Point out each Plasmodium parasite and each leukocyte.
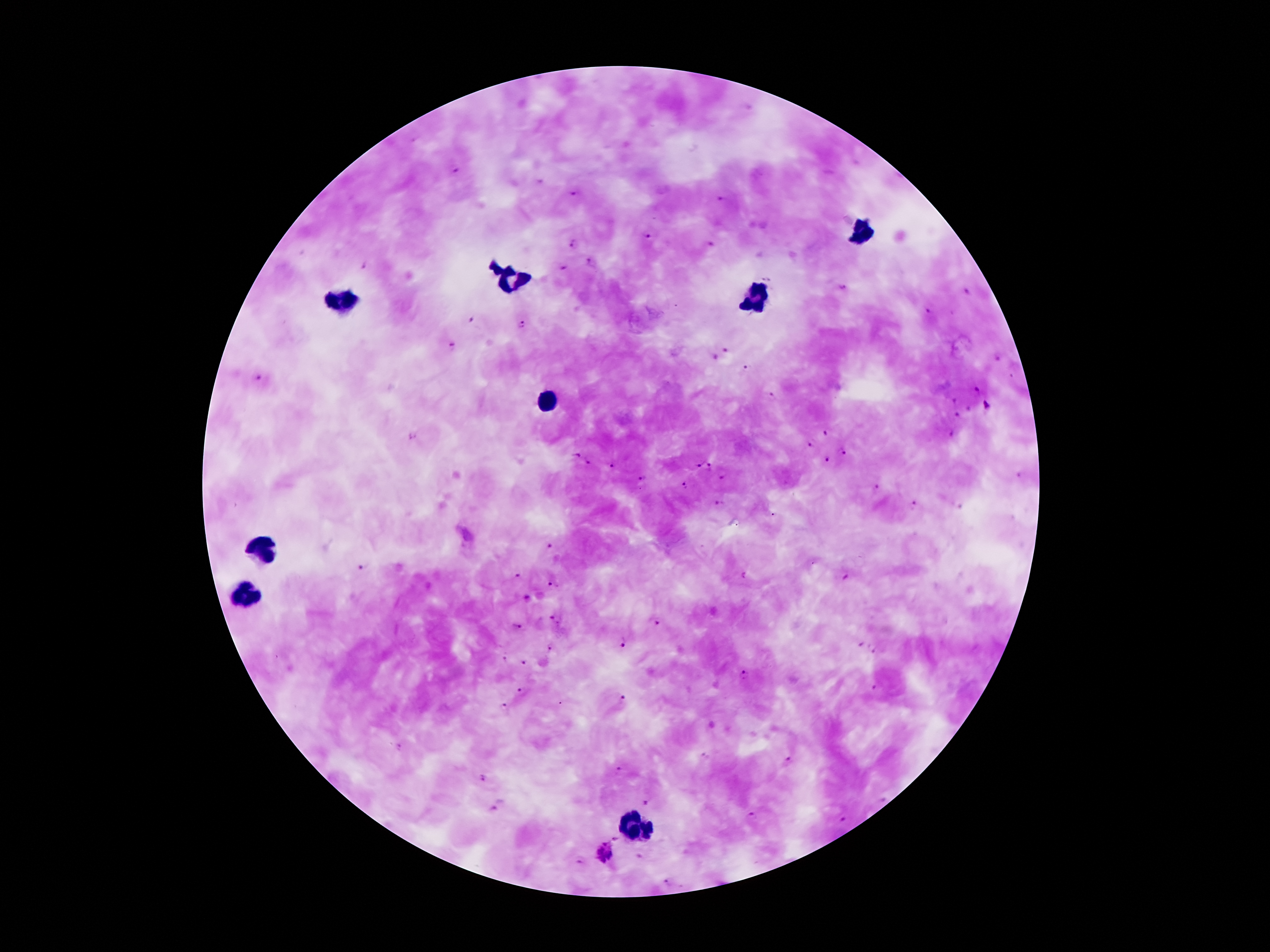
Approximate centers as {x, y} in pixels.
Plasmodium parasites: {457, 171}, {537, 182}, {572, 193}, {720, 198}, {650, 236}, {572, 242}, {712, 243}, {591, 262}, {364, 267}, {562, 267}, {842, 288}, {965, 293}, {926, 310}, {470, 320}, {523, 324}, {451, 345}, {725, 349}, {714, 356}, {998, 358}, {746, 368}, {1012, 375}, {259, 377}, {977, 387}, {772, 397}, {954, 401}, {987, 405}, {968, 409}, {957, 414}, {824, 431}, {950, 433}, {411, 435}, {810, 445}, {842, 453}, {575, 455}, {827, 459}, {587, 463}, {697, 464}, {613, 465}, {709, 466}, {642, 478}, {723, 478}, {686, 486}, {876, 487}, {913, 502}, {720, 503}, {958, 506}, {550, 545}, {360, 568}, {518, 574}, {743, 575}, {846, 579}, {551, 584}, {527, 598}, {554, 616}, {655, 621}, {520, 625}, {625, 642}, {551, 645}, {861, 645}, {875, 651}, {505, 658}, {525, 662}, {744, 676}, {875, 688}, {521, 692}, {621, 699}, {506, 706}, {703, 757}, {788, 759}, {617, 769}, {483, 778}, {644, 802}, {494, 807}, {752, 814}, {844, 819}, {617, 837}, {605, 850}, {639, 857}, {579, 862}, {666, 883}.
Leukocytes: {859, 233}, {509, 277}, {338, 298}, {756, 300}, {544, 403}, {261, 550}, {245, 594}, {635, 832}.

Giemsa-stained preparation. Image is 1270×952 pixels. 100x magnification. Thick blood film. Single field of view. Photographed through the microscope eyepiece with a smartphone camera. Patient malaria status: positive for Plasmodium falciparum.